Classify this cell by malaria status.
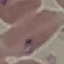

It is parasitized.

Thin blood smear. Giemsa stain. Cell patch, automatically extracted from a larger field of view and resized to 64 × 64 pixels. Acquired by smartphone through the microscope eyepiece.